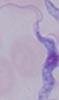

identification = trypanosome
magnification = 1000x
modality = micrograph